Classify this cell by malaria status.
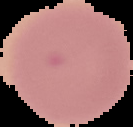

Uninfected.

Image is 133×127 pixels. Segmented cell region on a black background. From a thin blood smear.